Point out each Plasmodium parasite.
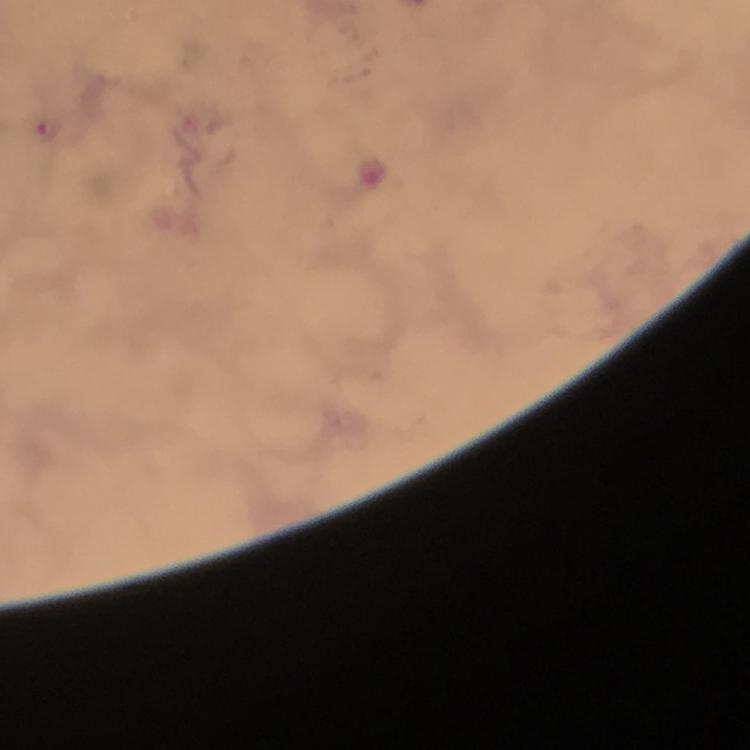

Approximate centers as [x, y] in pixels.
Plasmodium parasites: [50, 133].

magnification = 100x
cropped from = a single field of view
context = from a diagnostic examination for malaria
capture = smartphone photograph through a microscope
immersion oil = used
image size = 750×750 pixels
stain = Giemsa
preparation = thick blood film